Classify this cell by malaria status.
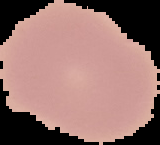
Uninfected.

Summary:
  - Image type: segmented cell region with the area outside set to black
  - Image size: 160×145 pixels
  - Preparation: thin blood smear